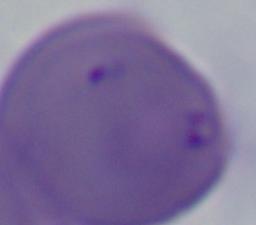

1000x magnification. Photomicrograph. A Babesia parasite is seen.